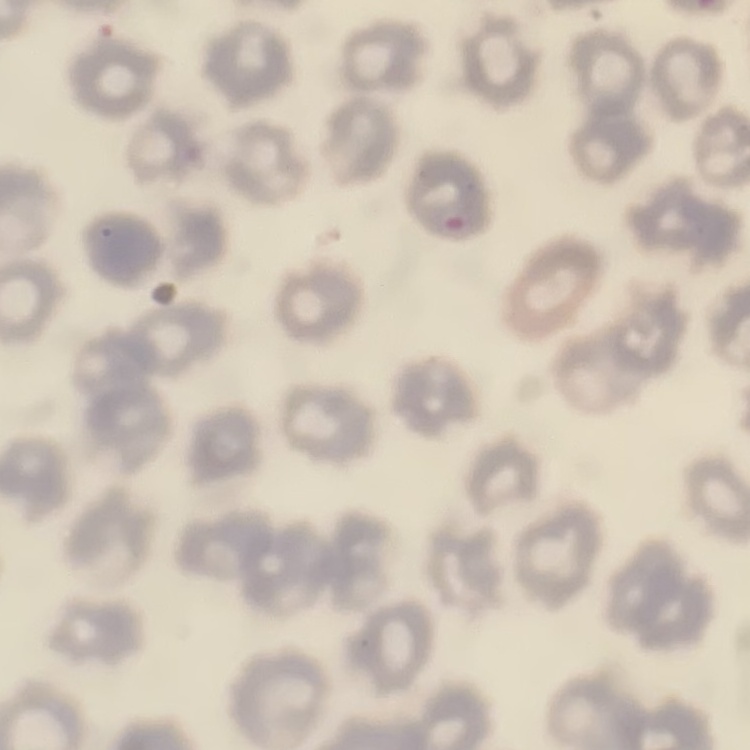
Summary:
  - Red blood cell morphology: no rouleaux formation
  - Image type: one tile cut from a larger photomicrograph
  - Stain: Field's or Giemsa
  - Preparation: thin blood film